Report the malaria status of this cell.
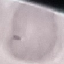
It is uninfected.

Acquired by smartphone through the microscope eyepiece. Thin blood smear. Automatically extracted cell patch, resized to 64 × 64 pixels. Giemsa-stained preparation.